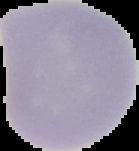
image type = segmented cell region with the area outside set to black
image size = 139×151 pixels
preparation = thin blood film
malaria status = uninfected